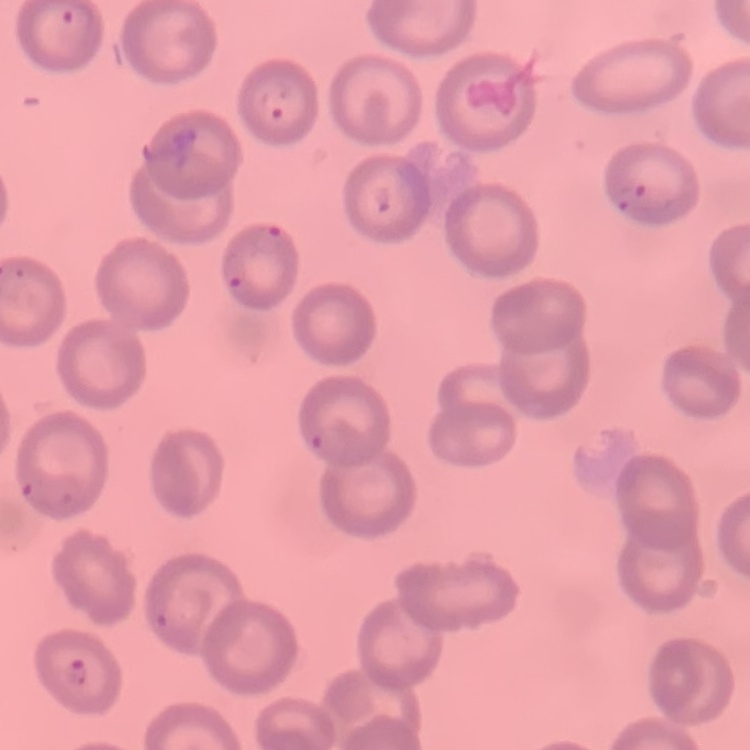
Summary:
  - Erythrocyte morphology: no rouleaux formation
  - Stain: Field's or Giemsa
  - Preparation: thin blood film
  - Image type: square crop of a larger photomicrograph